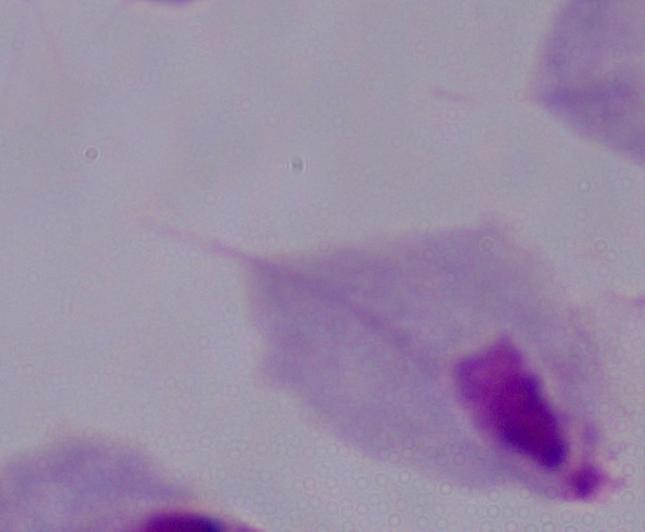
identification = trichomonad
modality = micrograph
magnification = 1000x